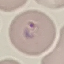
malaria status = parasitized
stain = Giemsa
capture = smartphone through the microscope eyepiece
image type = cell patch, automatically extracted from a larger field of view and resized to 64 × 64 pixels
preparation = thin blood film